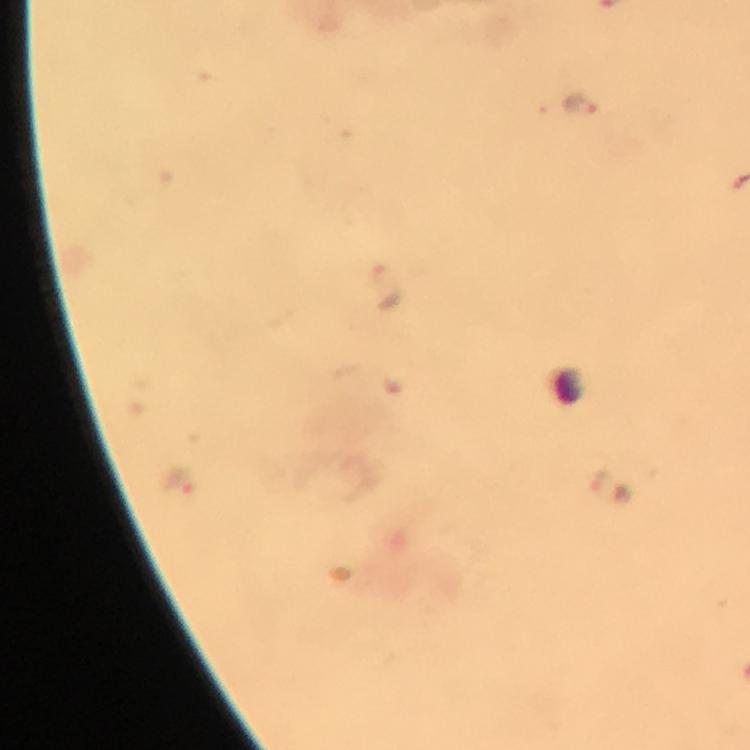

Approximate centers as [x, y] in pixels.
Summary:
  - Plasmodium parasite locations: [582, 104], [388, 288], [179, 481]
  - Cropped from: a single field of view
  - Context: from a malaria diagnostic workup
  - Magnification: 100x
  - Preparation: thick blood smear
  - Capture: smartphone camera through the microscope
  - Image size: 750×750 pixels
  - Stain: Giemsa
  - Immersion oil: used